Assess this cell for malaria.
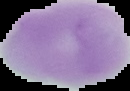
It is uninfected.

preparation: thin blood film
image_size: 130×91 pixels
image_type: segmented cell region with the area outside set to black